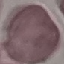 Malaria status: uninfected. Automatically extracted cell patch, resized to 64 × 64 pixels. Photographed with a smartphone camera at the microscope eyepiece. Thin smear of blood. Giemsa stain.